Give the extent of all Plasmodium malariae-infected red blood cells.
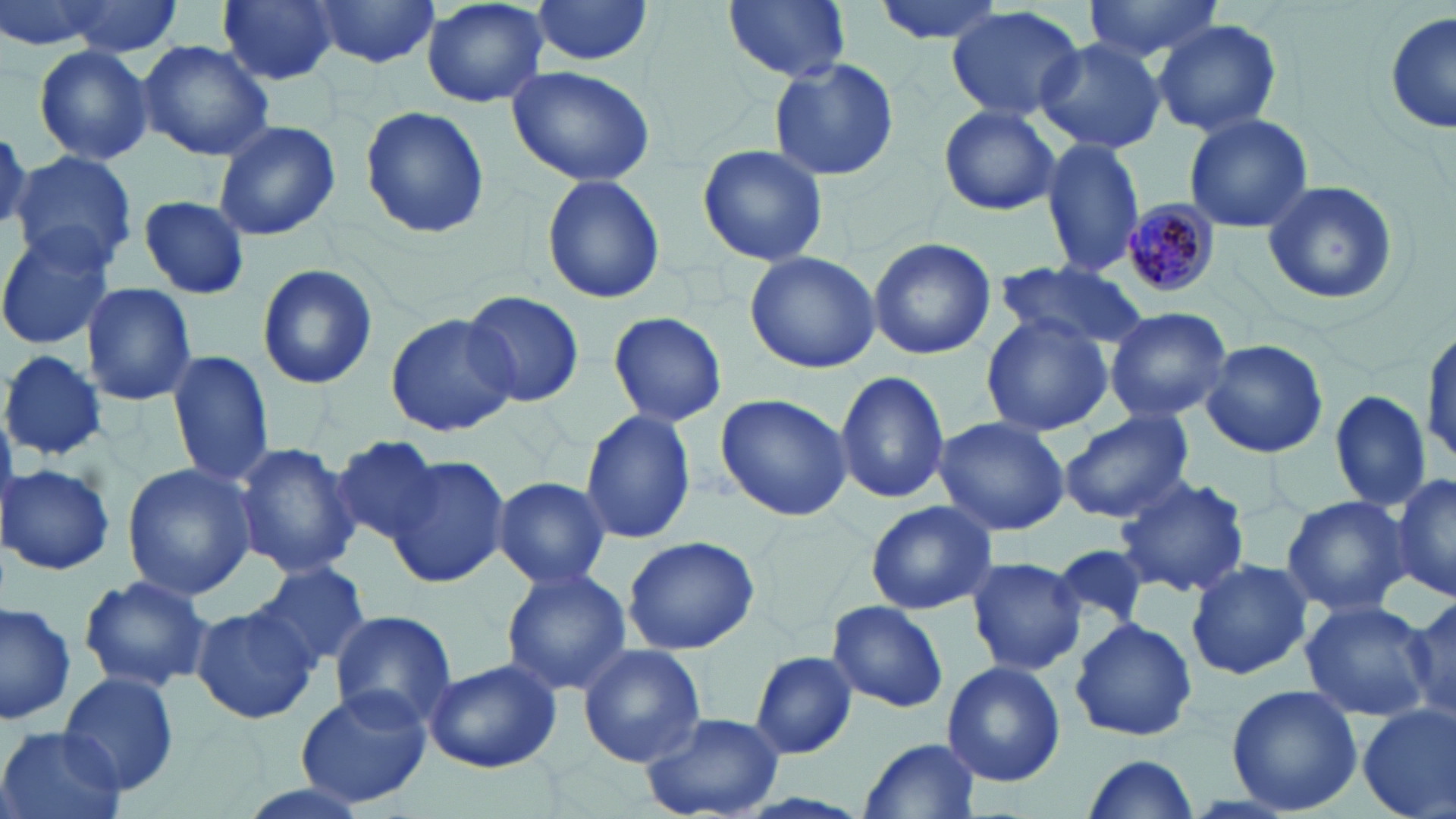

Approximate bounding boxes as [x1, y1, x2, y2] in pixels.
Plasmodium malariae-infected red blood cells: [1121, 199, 1221, 298].

slide-level diagnosis = Plasmodium malariae
stain = May-Grünwald-Giemsa
modality = light microscopy
field of view = one of a larger specimen
magnification = 1000x
preparation = thin blood smear
uninfected red blood cell locations = approximate bounding boxes as [x1, y1, x2, y2] in pixels: [42, 0, 187, 57], [218, 0, 339, 86], [306, 0, 441, 70], [422, 0, 549, 108], [529, 0, 657, 65], [724, 0, 851, 83], [870, 0, 1007, 46], [1085, 0, 1225, 63], [946, 5, 1085, 122], [1386, 13, 1455, 137], [1153, 19, 1282, 136], [1034, 37, 1168, 154], [138, 40, 274, 161], [32, 45, 156, 167], [769, 56, 899, 182], [506, 65, 657, 188], [360, 104, 490, 240], [938, 104, 1062, 215], [1182, 112, 1312, 233], [212, 120, 340, 243], [1042, 137, 1147, 278], [697, 142, 829, 267], [10, 150, 139, 272], [541, 171, 667, 305], [1261, 179, 1400, 307], [138, 195, 249, 299], [0, 227, 119, 350], [867, 238, 995, 360], [744, 250, 880, 375], [992, 260, 1148, 354], [257, 263, 378, 390], [80, 282, 197, 407], [461, 288, 586, 408], [1103, 306, 1232, 424], [606, 311, 728, 427], [386, 313, 516, 435], [981, 314, 1112, 437], [1421, 319, 1455, 468], [1201, 339, 1330, 460], [166, 349, 275, 488], [1, 350, 107, 459], [835, 369, 948, 506], [1330, 389, 1430, 513], [714, 392, 852, 524], [579, 409, 697, 544], [1057, 410, 1194, 523], [932, 416, 1069, 536], [331, 435, 445, 546], [232, 442, 360, 578], [388, 457, 511, 587], [3, 463, 116, 576], [121, 463, 260, 599], [1115, 474, 1250, 598], [1390, 474, 1455, 603], [491, 476, 611, 589], [1281, 494, 1411, 619], [865, 500, 996, 614], [620, 535, 763, 655], [1051, 542, 1150, 636], [966, 556, 1087, 676], [1185, 557, 1313, 680], [251, 561, 371, 673], [500, 567, 632, 696], [76, 573, 215, 696], [1405, 592, 1453, 721], [826, 599, 949, 714], [1299, 599, 1435, 722], [0, 602, 78, 726], [186, 605, 317, 724], [329, 610, 457, 729], [1069, 617, 1198, 742], [578, 644, 706, 767], [748, 650, 859, 759], [426, 658, 562, 774], [942, 661, 1065, 788], [61, 673, 181, 798], [1226, 684, 1362, 814], [295, 687, 432, 809], [1356, 703, 1456, 817], [639, 711, 785, 819], [1, 725, 124, 819], [860, 735, 981, 817], [1078, 755, 1200, 817], [221, 780, 384, 819]
image size = 1456×819 pixels